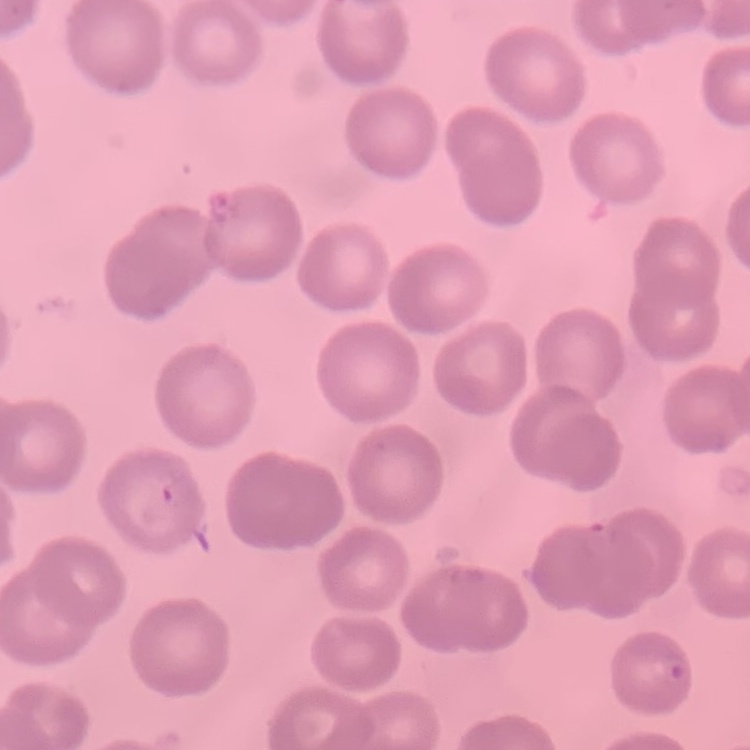
erythrocyte morphology = no rouleaux formation
preparation = thin peripheral smear
stain = Field's or Giemsa
image type = square crop of a larger photomicrograph